Name the parasite shown.
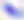
This is Toxoplasma gondii.

400x magnification. Micrograph.